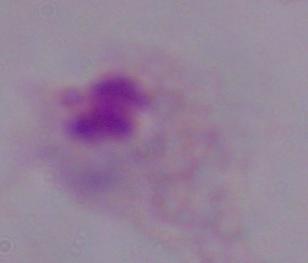

Summary:
  - Magnification: 1000x
  - Modality: micrograph
  - Identification: trichomonad